Report the malaria status of this cell.
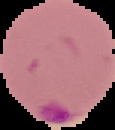

Parasitized.

preparation: thin blood smear
image_type: cell region segmented out of the field of view; surrounding area masked to black
image_size: 115×130 pixels